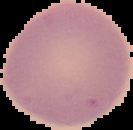 Image is 133×130 pixels. From a thin blood smear. Result: no Plasmodium parasites seen. Cell region segmented out of the field of view; the surrounding area is masked to black.